Name the parasite shown.
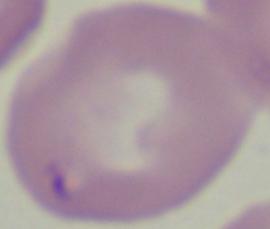

Babesia.

Summary:
  - Magnification: 1000x
  - Modality: micrograph